Identify the blood parasite species.
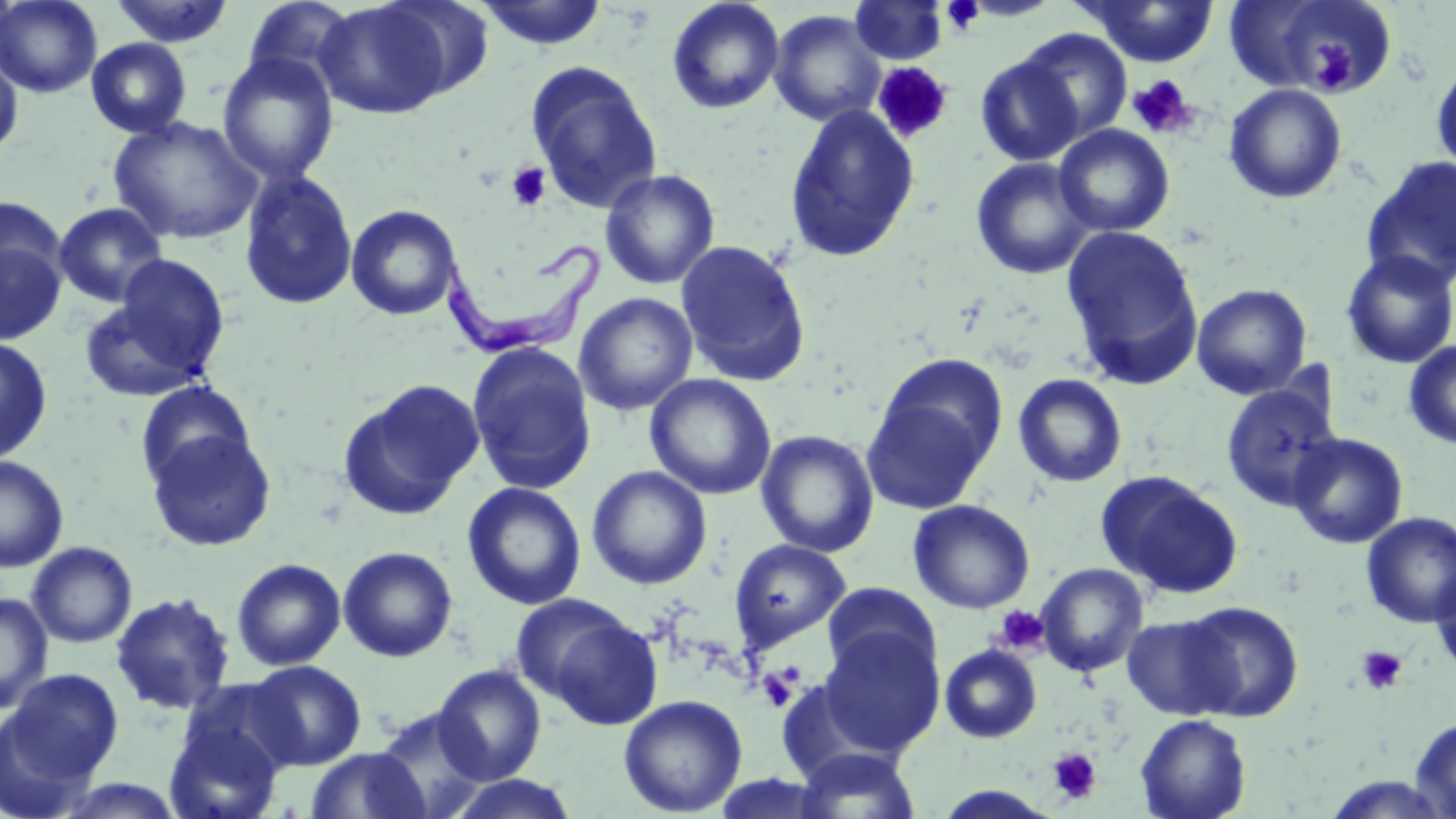
Trypanosoma brucei.

Approximate bounding boxes as (x1,y1)-(x2,y2) corner pairs in pixels. Platelet locations: (1308,42)-(1359,96), (873,62)-(953,144), (1127,74)-(1197,139), (505,162)-(551,212), (992,605)-(1050,655), (1355,645)-(1408,695), (758,667)-(799,713), (1047,746)-(1102,805). Uninfected red blood cell locations: (0,0)-(103,98), (242,0)-(358,90), (377,0)-(495,101), (849,0)-(948,65), (1080,0)-(1219,68), (1251,0)-(1392,95), (108,1)-(236,48), (314,1)-(454,119), (475,1)-(608,50), (666,1)-(785,114), (769,10)-(886,127), (1015,28)-(1133,145), (86,37)-(192,138), (0,47)-(23,159), (217,51)-(339,185), (975,55)-(1085,166), (1431,58)-(1456,176), (525,61)-(663,214), (1224,83)-(1348,204), (784,103)-(921,263), (108,115)-(264,246), (1054,124)-(1175,237), (1361,156)-(1456,288), (970,157)-(1096,280), (600,168)-(721,290), (238,169)-(358,312), (0,196)-(68,292), (53,202)-(168,308), (346,204)-(463,321), (1060,224)-(1204,388), (674,238)-(812,386), (0,239)-(66,345), (1340,250)-(1456,368), (109,254)-(232,377), (1191,283)-(1312,399), (573,292)-(698,416), (78,298)-(212,402), (0,336)-(52,465), (1403,339)-(1456,449), (466,341)-(598,495), (874,353)-(1007,476), (645,373)-(777,500), (1012,373)-(1128,487), (337,379)-(484,520), (135,380)-(255,488), (1219,382)-(1342,510), (858,392)-(996,516), (146,428)-(277,552), (756,429)-(879,557), (1288,432)-(1408,549), (0,455)-(68,572), (587,465)-(712,590), (1097,471)-(1242,599), (461,482)-(587,610), (908,499)-(1035,614), (1361,512)-(1456,628), (729,538)-(851,652), (27,542)-(137,648), (338,546)-(458,662), (231,558)-(346,671), (1035,562)-(1148,677), (1431,563)-(1456,681), (822,582)-(941,684), (0,591)-(53,715), (110,592)-(236,714), (1181,600)-(1304,723), (540,610)-(664,730), (1121,614)-(1238,720), (818,626)-(944,756), (939,644)-(1042,743), (245,660)-(367,770), (432,664)-(546,784), (5,669)-(124,784), (618,694)-(748,817), (0,706)-(96,819), (372,706)-(494,819), (1135,713)-(1251,819), (163,714)-(287,819), (1411,715)-(1456,817), (793,746)-(922,819), (305,747)-(433,818), (443,774)-(581,818), (1321,774)-(1455,818), (47,776)-(188,818), (933,785)-(1061,818). Trypanosoma brucei locations: (442,241)-(605,357). Light microscopy. One field of a larger specimen. Captured at 1000x magnification. Thin blood smear. Image is 1456×819 pixels. May-Grünwald-Giemsa-stained preparation.